State which parasite is depicted.
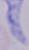
A trypanosome.

Captured at 1000x magnification. Photomicrograph.